Name the parasite shown.
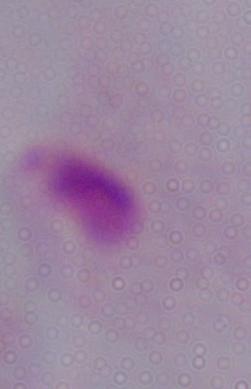

A trichomonad.

Micrograph. Captured at 1000x magnification.